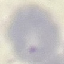

Summary:
  - Result: no malaria parasites seen
  - Stain: Giemsa
  - Capture: smartphone through the microscope eyepiece
  - Image type: automatically extracted cell patch, resized to 64 × 64 pixels
  - Preparation: thin blood film